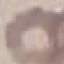

Result: no malaria parasites seen. Automatically extracted cell patch, resized to 64 × 64 pixels. Giemsa-stained preparation. Thin blood film. Acquired by smartphone through the microscope eyepiece.